Name the parasite shown.
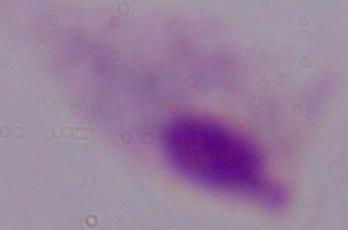
A trichomonad.

Summary:
  - Magnification: 1000x
  - Modality: micrograph